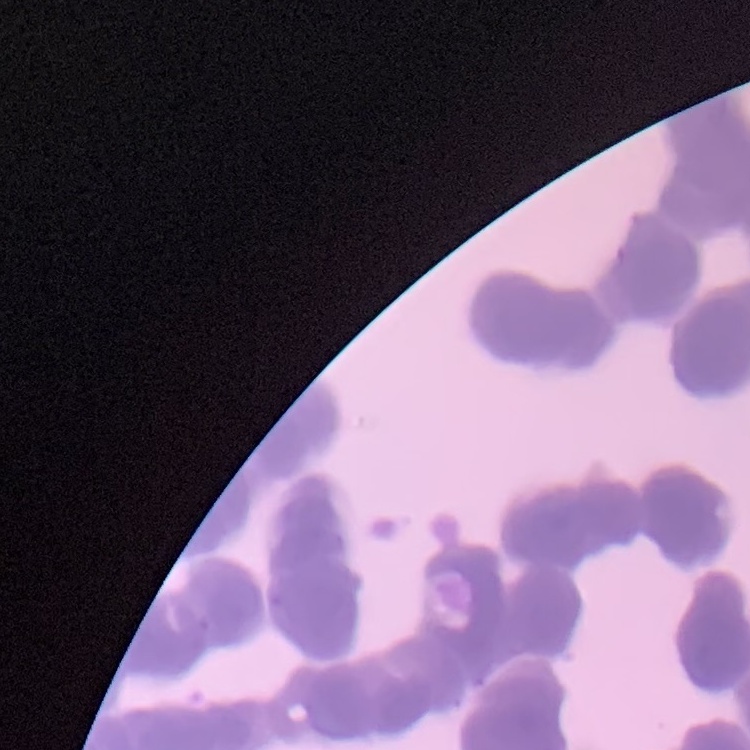

Summary:
  - Erythrocyte morphology: rouleaux formation
  - Image type: square crop of a larger photomicrograph
  - Preparation: thin blood smear
  - Stain: Field's or Giemsa